Locate leukocytes (white blood cells).
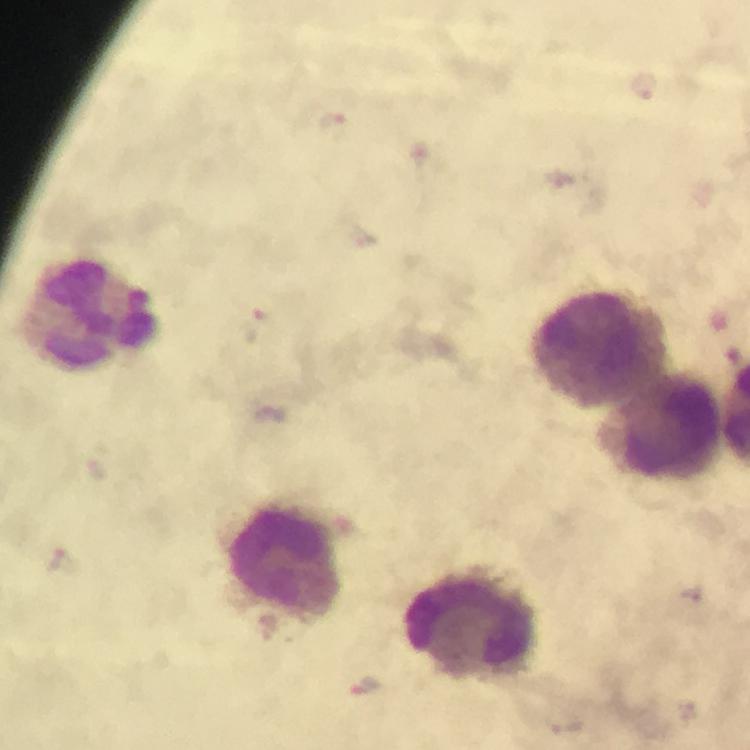

Approximate centers as (x, y) in pixels.
Leukocytes: (93, 317), (598, 350), (658, 428), (282, 560), (469, 628).

Plasmodium parasite locations: (645, 87), (333, 126), (257, 327), (274, 415), (65, 561), (692, 593), (367, 687). Photographed with a smartphone mounted on the microscope. Image is 750×750 pixels. Cropped region of a single field of view. Immersion oil was used. From a diagnostic examination for malaria. At 100x magnification. Thick blood smear. Giemsa stain.